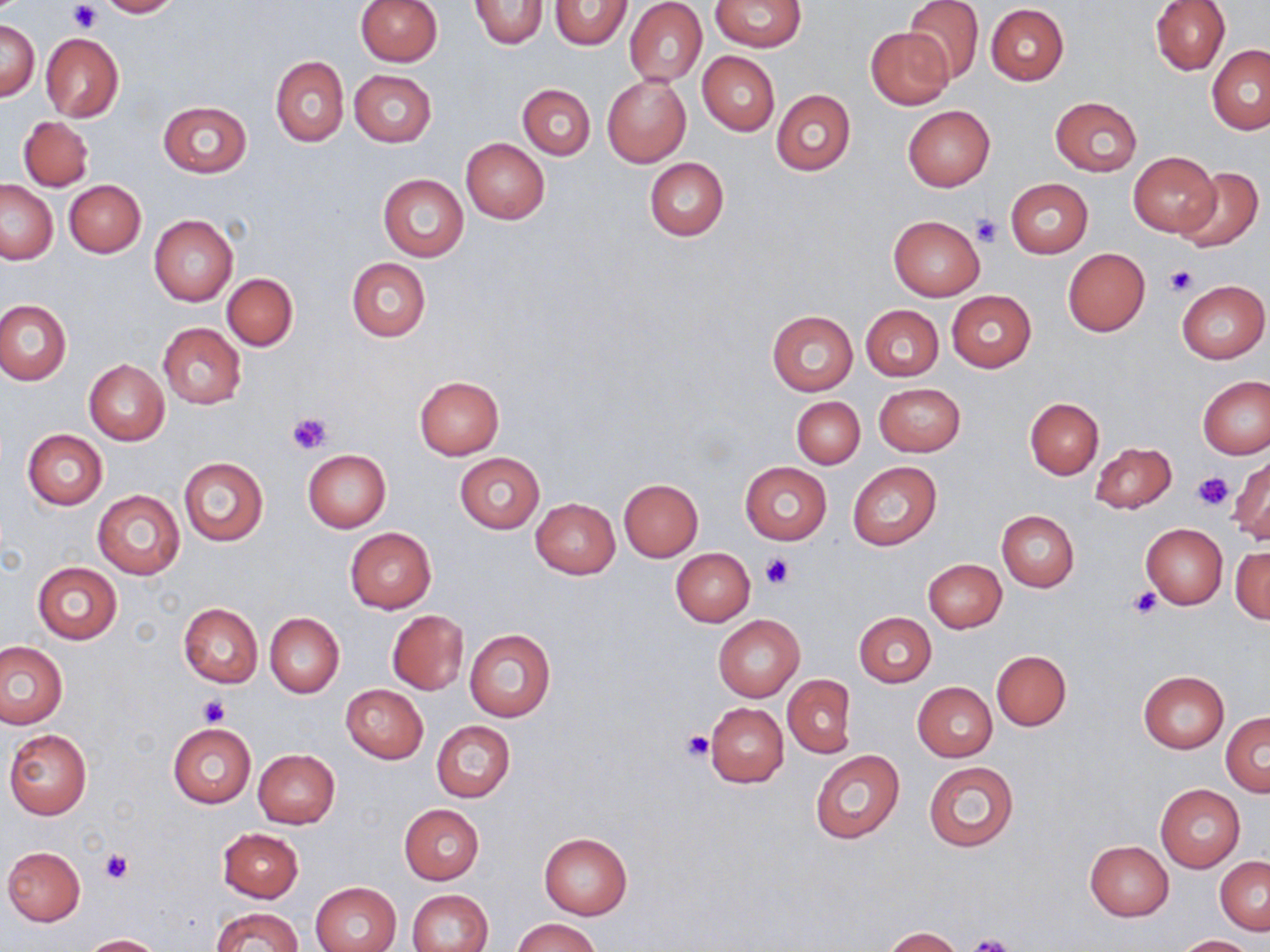
slide-level diagnosis = negative for blood parasites
platelet locations = approximate bounding boxes as named x1/y1/x2/y2 corners in pixels: (x1=68, y1=2, x2=100, y2=35), (x1=970, y1=215, x2=1003, y2=248), (x1=1165, y1=265, x2=1195, y2=296), (x1=288, y1=412, x2=332, y2=455), (x1=1189, y1=470, x2=1231, y2=512), (x1=760, y1=552, x2=795, y2=590), (x1=1129, y1=586, x2=1162, y2=617), (x1=199, y1=696, x2=228, y2=725), (x1=680, y1=727, x2=715, y2=763), (x1=99, y1=849, x2=133, y2=885), (x1=962, y1=936, x2=1017, y2=952)
preparation = thin blood smear
magnification = 1000x
image size = 1270×952 pixels
uninfected red blood cell locations = approximate bounding boxes as named x1/y1/x2/y2 corners in pixels: (x1=95, y1=0, x2=180, y2=17), (x1=356, y1=0, x2=442, y2=65), (x1=470, y1=0, x2=549, y2=48), (x1=710, y1=0, x2=806, y2=51), (x1=904, y1=0, x2=984, y2=83), (x1=1150, y1=0, x2=1230, y2=75), (x1=550, y1=1, x2=632, y2=50), (x1=624, y1=2, x2=707, y2=87), (x1=986, y1=4, x2=1070, y2=85), (x1=1, y1=19, x2=38, y2=101), (x1=865, y1=26, x2=954, y2=108), (x1=41, y1=33, x2=124, y2=122), (x1=1207, y1=45, x2=1270, y2=134), (x1=697, y1=52, x2=779, y2=135), (x1=271, y1=56, x2=348, y2=146), (x1=349, y1=70, x2=438, y2=147), (x1=603, y1=76, x2=690, y2=166), (x1=518, y1=84, x2=595, y2=159), (x1=771, y1=89, x2=854, y2=176), (x1=1050, y1=96, x2=1142, y2=176), (x1=158, y1=100, x2=252, y2=178), (x1=902, y1=106, x2=995, y2=190), (x1=18, y1=116, x2=94, y2=191), (x1=461, y1=138, x2=548, y2=223), (x1=1127, y1=151, x2=1221, y2=236), (x1=644, y1=157, x2=729, y2=240), (x1=1176, y1=167, x2=1263, y2=252), (x1=378, y1=174, x2=468, y2=261), (x1=1005, y1=178, x2=1093, y2=258), (x1=64, y1=180, x2=145, y2=258), (x1=0, y1=181, x2=57, y2=264), (x1=149, y1=214, x2=237, y2=306), (x1=888, y1=215, x2=984, y2=300), (x1=1063, y1=248, x2=1151, y2=336), (x1=346, y1=257, x2=430, y2=342), (x1=222, y1=273, x2=298, y2=350), (x1=1177, y1=279, x2=1268, y2=363), (x1=946, y1=290, x2=1036, y2=372), (x1=0, y1=300, x2=72, y2=386), (x1=860, y1=305, x2=943, y2=380), (x1=766, y1=310, x2=857, y2=394), (x1=158, y1=324, x2=246, y2=409), (x1=83, y1=360, x2=170, y2=444), (x1=415, y1=375, x2=504, y2=458), (x1=1198, y1=376, x2=1270, y2=459), (x1=873, y1=382, x2=965, y2=456), (x1=791, y1=396, x2=865, y2=469), (x1=1025, y1=398, x2=1104, y2=479), (x1=23, y1=429, x2=107, y2=510), (x1=1090, y1=441, x2=1178, y2=514), (x1=303, y1=450, x2=390, y2=532), (x1=455, y1=453, x2=545, y2=534), (x1=1230, y1=454, x2=1270, y2=544), (x1=179, y1=457, x2=268, y2=547), (x1=740, y1=461, x2=833, y2=544), (x1=847, y1=462, x2=941, y2=549), (x1=619, y1=479, x2=703, y2=561), (x1=92, y1=490, x2=184, y2=579), (x1=531, y1=498, x2=620, y2=579), (x1=997, y1=510, x2=1079, y2=592), (x1=1141, y1=524, x2=1228, y2=609), (x1=344, y1=527, x2=437, y2=613), (x1=1231, y1=546, x2=1270, y2=623), (x1=671, y1=547, x2=755, y2=626), (x1=924, y1=559, x2=1006, y2=633), (x1=33, y1=562, x2=122, y2=643), (x1=177, y1=604, x2=262, y2=688), (x1=387, y1=610, x2=469, y2=694), (x1=854, y1=611, x2=936, y2=688), (x1=265, y1=613, x2=344, y2=698), (x1=713, y1=615, x2=805, y2=701), (x1=464, y1=628, x2=556, y2=723), (x1=0, y1=642, x2=67, y2=728), (x1=991, y1=650, x2=1071, y2=731), (x1=1138, y1=670, x2=1230, y2=753), (x1=784, y1=675, x2=855, y2=758), (x1=913, y1=682, x2=997, y2=761), (x1=341, y1=684, x2=428, y2=763), (x1=705, y1=702, x2=789, y2=788), (x1=1221, y1=713, x2=1270, y2=796), (x1=431, y1=720, x2=515, y2=803), (x1=168, y1=723, x2=255, y2=807), (x1=4, y1=729, x2=92, y2=819), (x1=252, y1=749, x2=339, y2=828), (x1=809, y1=749, x2=904, y2=845), (x1=923, y1=760, x2=1019, y2=852), (x1=1155, y1=784, x2=1246, y2=873), (x1=400, y1=805, x2=483, y2=884), (x1=217, y1=827, x2=304, y2=903), (x1=539, y1=833, x2=632, y2=919), (x1=1084, y1=841, x2=1174, y2=921), (x1=3, y1=846, x2=85, y2=925), (x1=1216, y1=855, x2=1270, y2=935), (x1=310, y1=882, x2=401, y2=952), (x1=406, y1=889, x2=492, y2=952), (x1=211, y1=907, x2=301, y2=952), (x1=513, y1=918, x2=600, y2=952), (x1=883, y1=927, x2=964, y2=952), (x1=82, y1=934, x2=163, y2=951), (x1=1175, y1=935, x2=1255, y2=952)
modality = optical microscopy
field of view = one of a larger specimen
stain = May-Grünwald-Giemsa